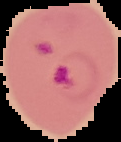

Summary:
  - Image size: 121×142 pixels
  - Image type: cell region segmented out of the field of view; surrounding area masked to black
  - Result: Plasmodium parasites detected
  - Preparation: thin blood film